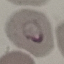
Summary:
  - Malaria status: parasitized
  - Stain: Giemsa
  - Capture: smartphone through the microscope eyepiece
  - Preparation: thin blood smear
  - Image type: automatically extracted cell patch, resized to 64 × 64 pixels